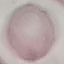

Result: negative for malaria parasites. Automatically extracted cell patch, resized to 64 × 64 pixels. Photographed with a smartphone camera at the microscope eyepiece. Giemsa stain. Thin smear of blood.